Outline each blood parasite and name the species.
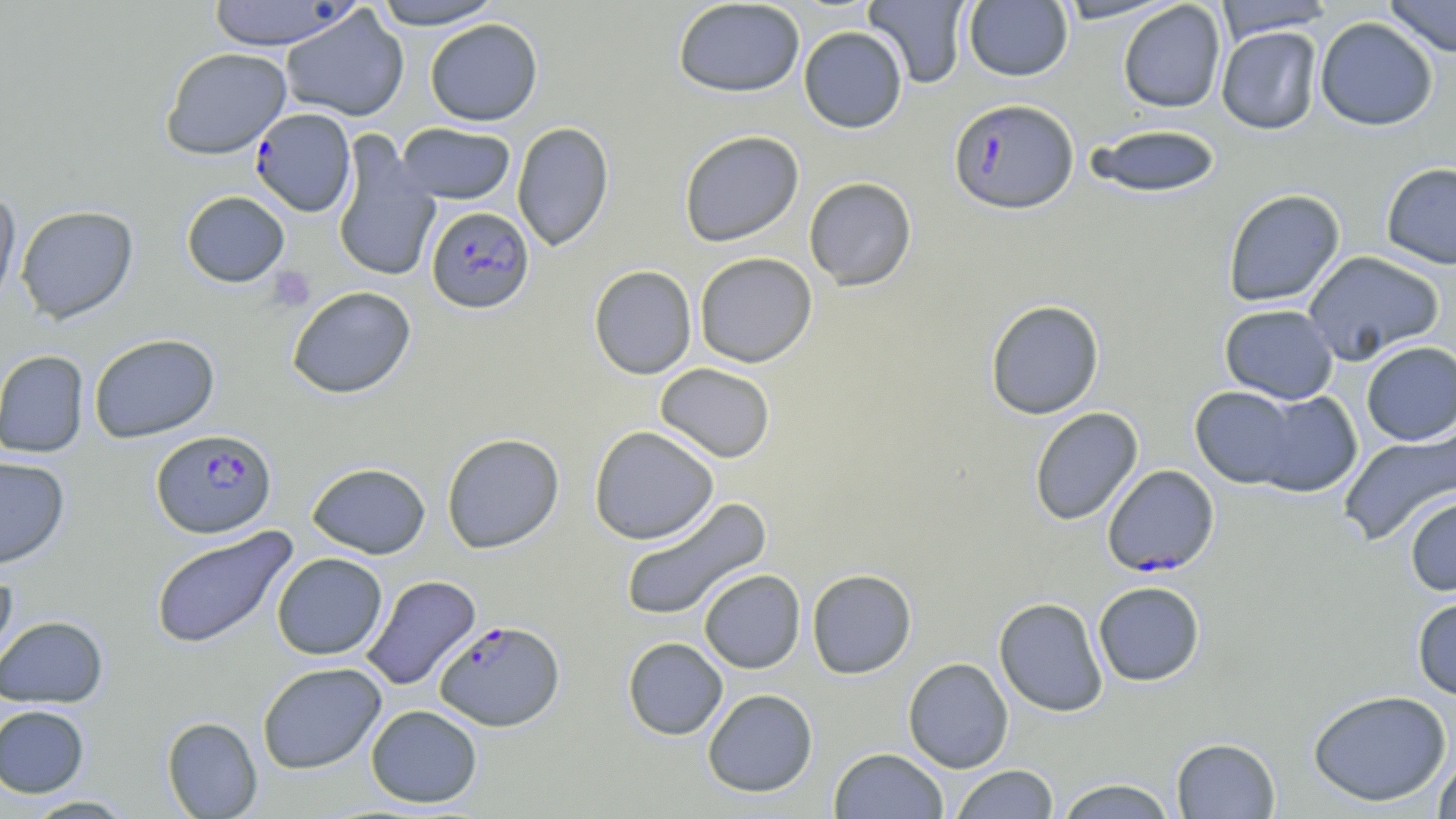

Approximate bounding boxes as (x1, y1, x2, y2) in pixels.
Plasmodium falciparum-infected red blood cells: (949, 98, 1078, 214), (250, 108, 356, 217), (426, 206, 534, 313), (151, 428, 277, 538), (1102, 464, 1220, 576), (434, 620, 565, 731).
No Plasmodium ovale, Plasmodium malariae, Plasmodium vivax, Babesia divergens, or Trypanosoma brucei observed.

Platelet locations: (267, 266, 316, 312). Uninfected red blood cell locations: (205, 0, 356, 50), (370, 0, 505, 30), (672, 0, 806, 98), (863, 0, 972, 88), (1052, 0, 1183, 24), (1383, 0, 1456, 58), (963, 1, 1073, 82), (1117, 1, 1226, 113), (1214, 1, 1335, 40), (280, 6, 410, 122), (1315, 17, 1438, 131), (424, 18, 543, 126), (798, 26, 908, 133), (1216, 26, 1322, 134), (160, 47, 291, 159), (511, 121, 614, 251), (396, 123, 516, 204), (1084, 123, 1222, 197), (678, 129, 804, 247), (332, 131, 441, 284), (1381, 162, 1456, 270), (803, 176, 917, 291), (1222, 189, 1345, 307), (0, 190, 21, 315), (181, 190, 290, 287), (15, 205, 138, 324), (1302, 250, 1445, 365), (694, 252, 817, 368), (588, 265, 697, 380), (287, 285, 416, 399), (985, 299, 1105, 420), (1219, 304, 1339, 404), (89, 333, 219, 443), (1361, 341, 1456, 446), (0, 349, 89, 458), (654, 363, 776, 463), (1188, 386, 1304, 487), (1241, 389, 1363, 497), (1029, 406, 1143, 526), (588, 425, 719, 545), (1337, 427, 1456, 546), (441, 433, 564, 554), (0, 456, 70, 568), (306, 462, 431, 559), (1404, 493, 1456, 596), (619, 497, 772, 623), (150, 527, 298, 648), (271, 552, 387, 660), (0, 567, 18, 677), (806, 568, 917, 679), (699, 569, 805, 673), (360, 574, 481, 691), (1092, 581, 1206, 687), (1411, 594, 1456, 700), (993, 597, 1108, 717), (0, 615, 109, 708), (622, 637, 728, 740), (903, 657, 1014, 773), (257, 662, 387, 774), (702, 688, 818, 797), (1308, 689, 1452, 807), (0, 704, 90, 798), (366, 704, 483, 808), (162, 716, 262, 818), (1171, 737, 1280, 818), (828, 747, 949, 819), (1432, 755, 1456, 818), (950, 764, 1059, 818), (1053, 778, 1179, 819), (21, 795, 138, 818). Slide-level diagnosis: Plasmodium falciparum. Light microscopy. Image is 1456×819 pixels. One field of a larger specimen. Captured at 1000x magnification. Thin blood smear. May-Grünwald-Giemsa stain.